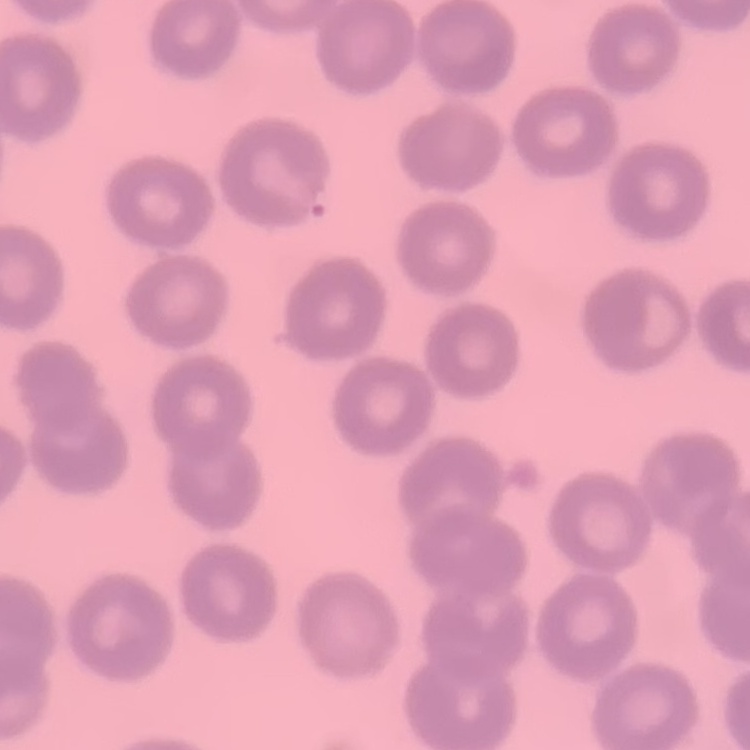
{
  "erythrocyte_morphology": "no rouleaux formation",
  "stain": "Field's or Giemsa",
  "preparation": "thin blood film",
  "image_type": "square crop of a larger photomicrograph"
}